Name the blood parasite species.
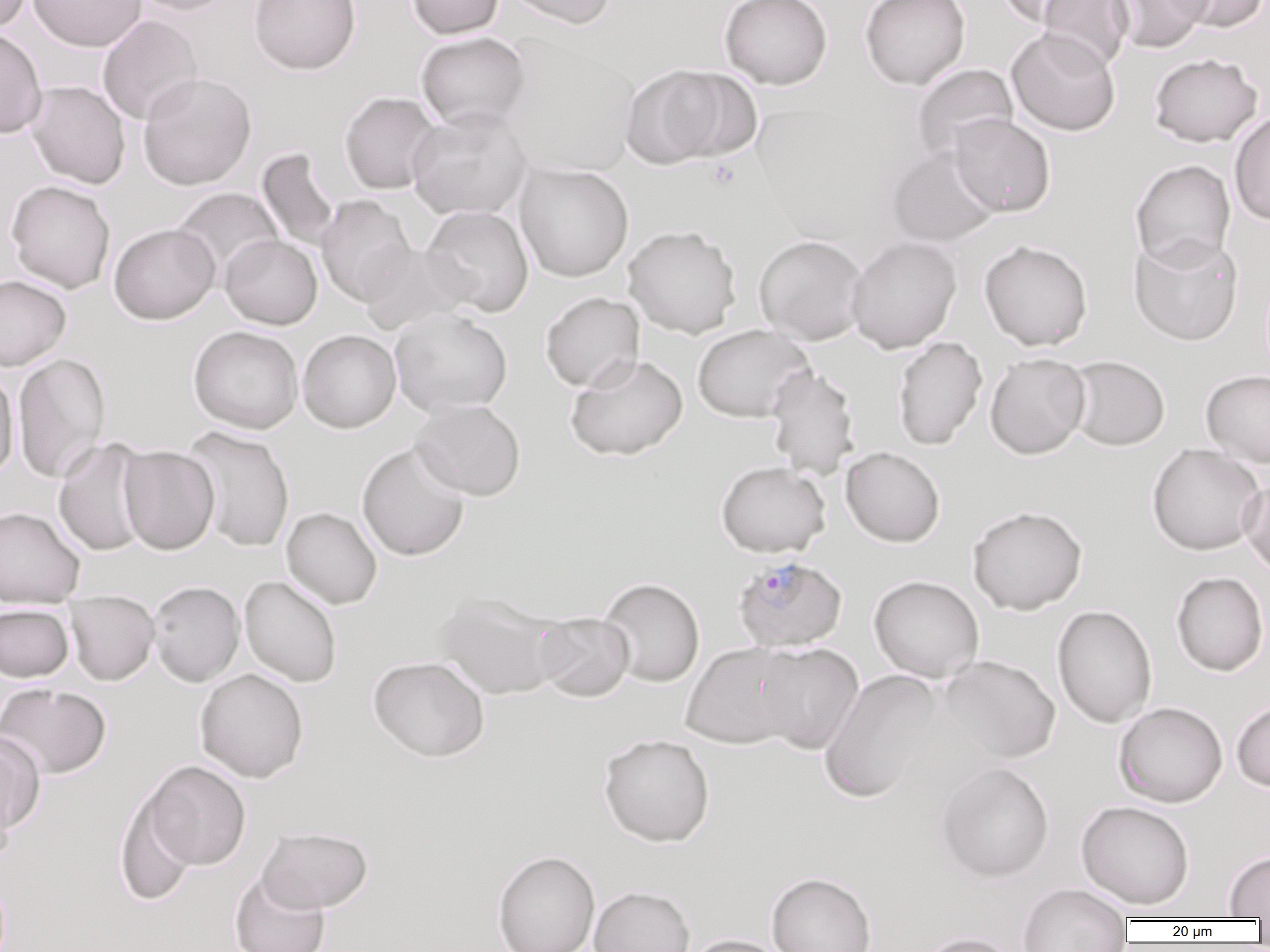

Plasmodium falciparum.

Approximate bounding boxes as (x1,y1)-(x2,y2) corner pairs in pixels. Platelet locations: (706,159)-(741,191). Uninfected red blood cell locations: (0,0)-(33,34), (28,0)-(147,52), (130,0)-(238,16), (248,0)-(362,76), (405,0)-(505,39), (504,0)-(617,30), (719,0)-(833,90), (860,0)-(971,90), (994,0)-(1100,28), (1037,0)-(1133,71), (1107,0)-(1211,54), (1165,0)-(1269,33), (97,15)-(202,125), (0,27)-(48,139), (1006,28)-(1121,136), (415,32)-(532,132), (501,37)-(641,179), (1148,53)-(1262,147), (910,64)-(1018,165), (620,65)-(740,168), (137,72)-(257,190), (25,80)-(131,189), (339,91)-(442,194), (407,106)-(533,220), (1229,110)-(1270,227), (949,113)-(1055,217), (887,146)-(1001,248), (255,148)-(343,253), (1130,159)-(1236,271), (515,163)-(634,282), (5,180)-(115,293), (172,187)-(284,283), (316,195)-(417,306), (421,205)-(534,316), (108,223)-(220,324), (623,225)-(741,338), (221,234)-(322,329), (1129,234)-(1244,345), (753,235)-(869,344), (846,236)-(962,353), (978,239)-(1093,351), (356,242)-(470,334), (0,274)-(71,370), (541,292)-(645,392), (389,307)-(513,417), (692,324)-(815,422), (188,326)-(303,433), (298,330)-(401,432), (893,336)-(987,450), (12,351)-(111,484), (985,353)-(1091,459), (565,354)-(688,461), (1065,356)-(1170,451), (765,365)-(860,479), (0,367)-(19,483), (1201,370)-(1270,468), (411,399)-(526,500), (182,426)-(295,552), (52,438)-(153,557), (356,442)-(471,562), (1145,443)-(1267,556), (118,446)-(219,555), (841,447)-(945,547), (716,461)-(831,557), (1239,476)-(1270,579), (966,505)-(1088,615), (0,506)-(85,606), (281,507)-(382,609), (1170,571)-(1269,676), (240,575)-(342,688), (868,575)-(985,683), (598,577)-(705,687), (148,581)-(245,687), (432,591)-(566,700), (65,592)-(160,686), (0,604)-(74,682), (1052,604)-(1157,729), (534,611)-(635,703), (681,642)-(804,748), (756,643)-(863,754), (937,655)-(1061,765), (367,656)-(489,762), (195,668)-(309,783), (818,669)-(945,803), (0,682)-(112,779), (1231,698)-(1270,792), (1113,702)-(1228,808), (0,730)-(45,837), (598,733)-(715,847), (142,761)-(251,870), (936,762)-(1055,882), (0,774)-(15,870), (115,786)-(200,908), (1076,800)-(1195,909), (256,826)-(373,913), (491,850)-(600,952), (1223,851)-(1270,919), (229,871)-(331,952), (766,872)-(877,952), (1018,883)-(1132,951), (589,885)-(695,952), (916,932)-(1020,952), (684,934)-(791,952). Plasmodium falciparum-infected red blood cell locations: (732,555)-(848,653). Thin blood film. Light microscopy. Captured at 1000x magnification. Single field of view. Image is 1270×952 pixels.